Name the cell type shown.
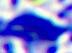
This is a leukocyte.

Captured at 400x magnification. Micrograph.